Comment on the morphology of the erythrocytes.
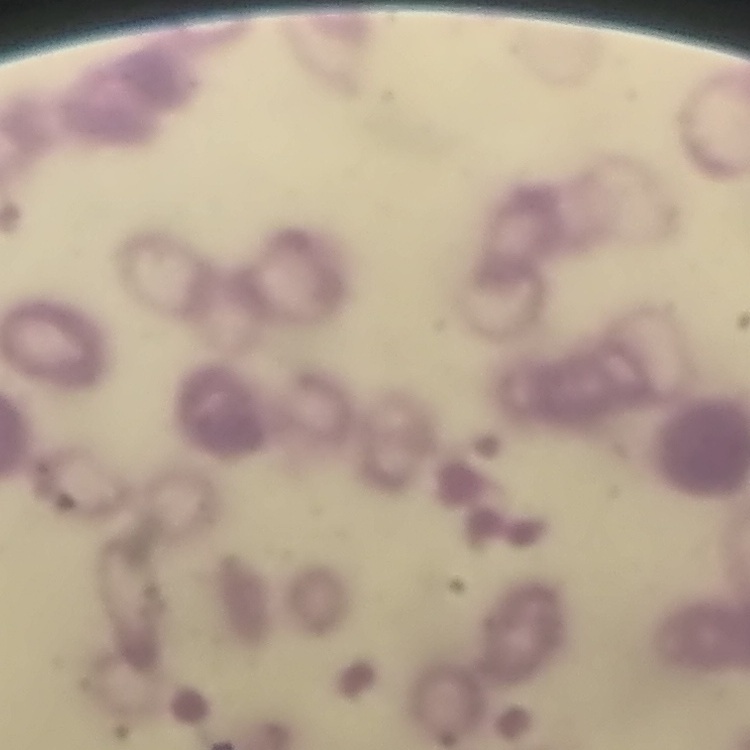
They show rouleaux formation.

Summary:
  - Image type: square crop of a larger photomicrograph
  - Stain: Field's or Giemsa
  - Preparation: thin blood film